State the blood parasite species.
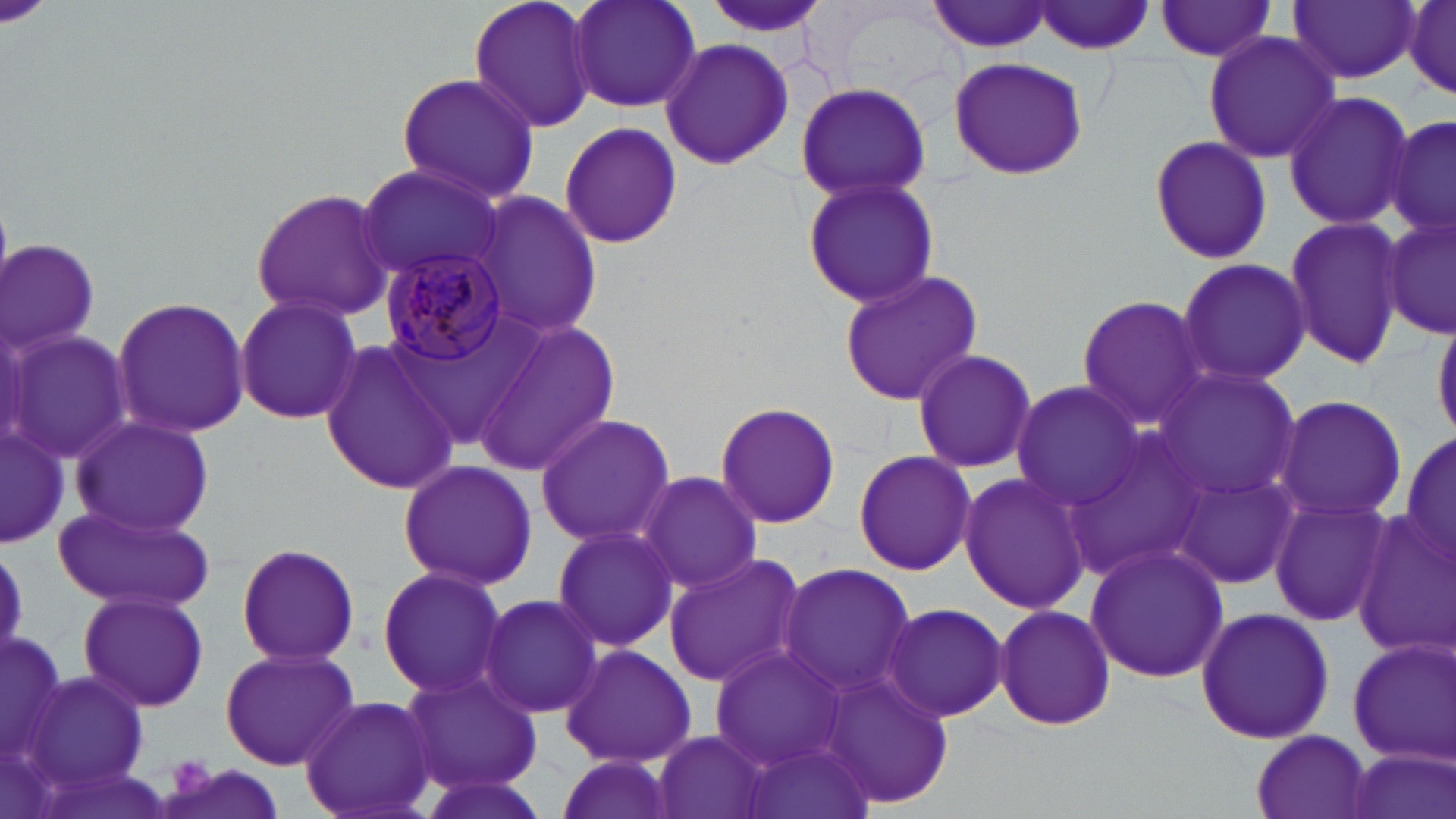

Plasmodium malariae.

Summary:
  - Coordinate format: approximate bounding boxes as named x1/y1/x2/y2 corners in pixels
  - Plasmodium malariae-infected red blood cell locations: (x1=380, y1=249, x2=511, y2=366)
  - Uninfected red blood cell locations: (x1=468, y1=0, x2=600, y2=137), (x1=563, y1=0, x2=704, y2=116), (x1=1287, y1=0, x2=1421, y2=85), (x1=928, y1=1, x2=1057, y2=53), (x1=1033, y1=1, x2=1158, y2=55), (x1=1152, y1=2, x2=1281, y2=62), (x1=1401, y1=2, x2=1456, y2=98), (x1=1203, y1=29, x2=1342, y2=165), (x1=657, y1=37, x2=795, y2=172), (x1=943, y1=54, x2=1089, y2=181), (x1=395, y1=71, x2=539, y2=205), (x1=794, y1=81, x2=933, y2=205), (x1=1282, y1=91, x2=1413, y2=231), (x1=1386, y1=110, x2=1455, y2=242), (x1=557, y1=120, x2=684, y2=249), (x1=1147, y1=135, x2=1273, y2=265), (x1=356, y1=166, x2=506, y2=291), (x1=799, y1=174, x2=943, y2=308), (x1=250, y1=185, x2=393, y2=323), (x1=472, y1=188, x2=603, y2=344), (x1=1380, y1=211, x2=1455, y2=343), (x1=1281, y1=214, x2=1403, y2=369), (x1=2, y1=238, x2=99, y2=361), (x1=1173, y1=257, x2=1312, y2=389), (x1=837, y1=269, x2=986, y2=409), (x1=234, y1=294, x2=364, y2=426), (x1=1075, y1=294, x2=1210, y2=431), (x1=111, y1=296, x2=252, y2=438), (x1=474, y1=319, x2=622, y2=476), (x1=7, y1=331, x2=133, y2=464), (x1=319, y1=335, x2=465, y2=494), (x1=913, y1=348, x2=1036, y2=474), (x1=1156, y1=368, x2=1302, y2=503), (x1=1008, y1=381, x2=1145, y2=511), (x1=1273, y1=393, x2=1408, y2=525), (x1=713, y1=402, x2=841, y2=530), (x1=533, y1=413, x2=674, y2=547), (x1=67, y1=414, x2=215, y2=539), (x1=0, y1=422, x2=69, y2=548), (x1=1400, y1=425, x2=1454, y2=572), (x1=1063, y1=428, x2=1209, y2=579), (x1=852, y1=450, x2=978, y2=576), (x1=396, y1=459, x2=538, y2=591), (x1=1172, y1=466, x2=1303, y2=589), (x1=635, y1=470, x2=762, y2=595), (x1=957, y1=471, x2=1092, y2=615), (x1=1271, y1=499, x2=1394, y2=626), (x1=54, y1=503, x2=213, y2=612), (x1=1351, y1=508, x2=1453, y2=655), (x1=551, y1=522, x2=678, y2=653), (x1=234, y1=541, x2=361, y2=667), (x1=1083, y1=541, x2=1228, y2=685), (x1=0, y1=544, x2=32, y2=660), (x1=662, y1=552, x2=807, y2=689), (x1=776, y1=560, x2=919, y2=696), (x1=377, y1=564, x2=510, y2=698), (x1=79, y1=589, x2=211, y2=713), (x1=478, y1=593, x2=602, y2=719), (x1=879, y1=601, x2=1009, y2=722), (x1=993, y1=605, x2=1117, y2=730), (x1=1194, y1=606, x2=1335, y2=745), (x1=0, y1=625, x2=66, y2=770), (x1=1347, y1=637, x2=1455, y2=762), (x1=559, y1=643, x2=698, y2=768), (x1=708, y1=645, x2=850, y2=768), (x1=219, y1=646, x2=362, y2=770), (x1=397, y1=665, x2=544, y2=797), (x1=823, y1=668, x2=955, y2=810), (x1=24, y1=669, x2=152, y2=797), (x1=299, y1=694, x2=440, y2=819), (x1=650, y1=729, x2=775, y2=819), (x1=1251, y1=731, x2=1374, y2=818), (x1=739, y1=735, x2=878, y2=819), (x1=1347, y1=751, x2=1452, y2=819), (x1=552, y1=752, x2=674, y2=819), (x1=157, y1=762, x2=287, y2=819), (x1=415, y1=770, x2=552, y2=819)
  - Preparation: thin blood smear
  - Image size: 1456×819 pixels
  - Modality: light microscopy
  - Magnification: 1000x
  - Field of view: single
  - Stain: May-Grünwald-Giemsa